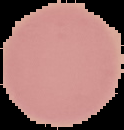
Summary:
  - Preparation: thin blood film
  - Image size: 124×130 pixels
  - Image type: cell region segmented out of the field of view; surrounding area masked to black
  - Malaria status: uninfected